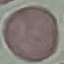
{
  "malaria_status": "uninfected",
  "image_type": "automatically extracted cell patch, resized to 64 × 64 pixels",
  "preparation": "thin blood smear",
  "capture": "smartphone through the microscope eyepiece",
  "stain": "Giemsa"
}